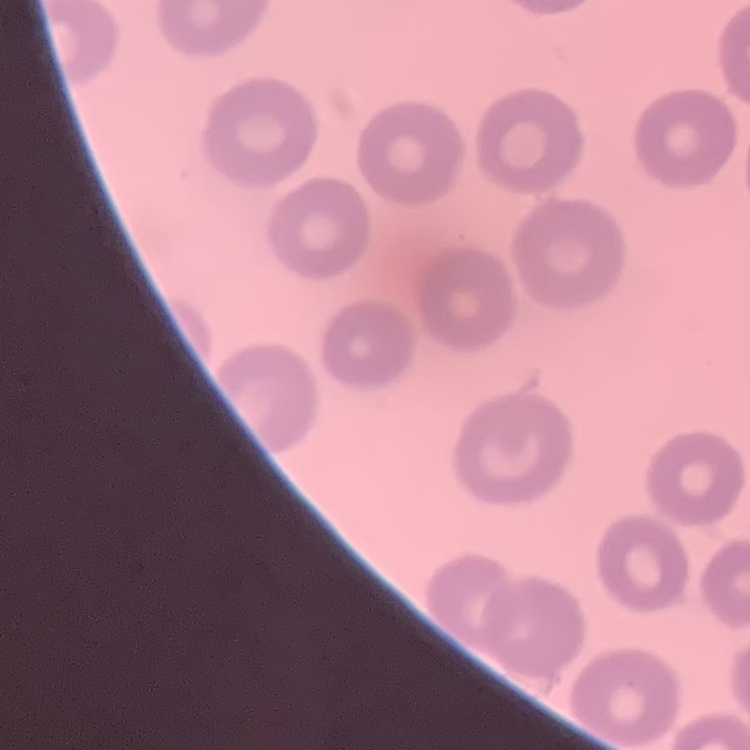
Summary:
  - Erythrocyte morphology: no rouleaux formation
  - Preparation: thin peripheral smear
  - Stain: Field's or Giemsa
  - Image type: one tile cut from a larger photomicrograph